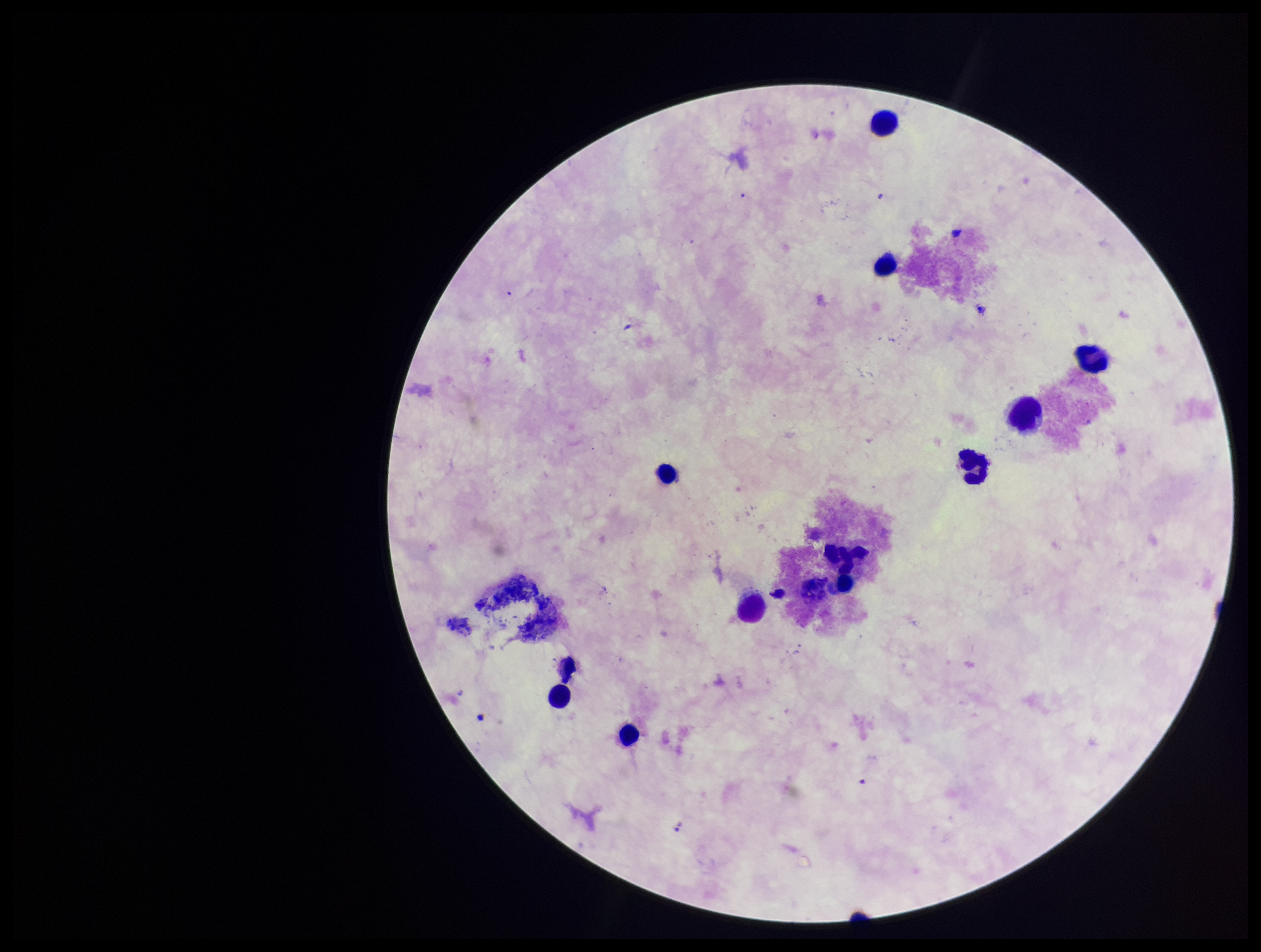
Plasmodium parasites = none detected
patient malaria status = negative
leukocyte count = 11
image size = 1261×952 pixels
stain = Giemsa
preparation = thick smear
parasite count = 0
capture = smartphone photograph through the microscope eyepiece
field of view = single